Comment on the morphology of the erythrocytes.
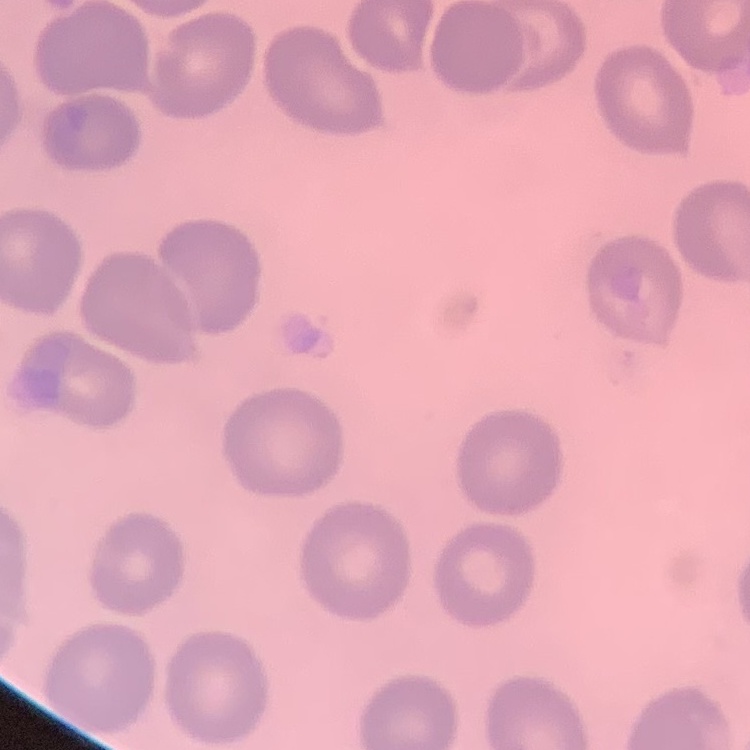

No rouleaux formation.

preparation = thin blood film
image type = one tile cut from a larger photomicrograph
stain = Field's or Giemsa